Report the malaria status of this cell.
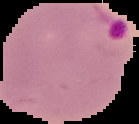

Parasitized.

{
  "image_size": "139×124 pixels",
  "image_type": "segmented cell region on a black background",
  "preparation": "thin blood smear"
}